Describe the morphology of the red blood cells.
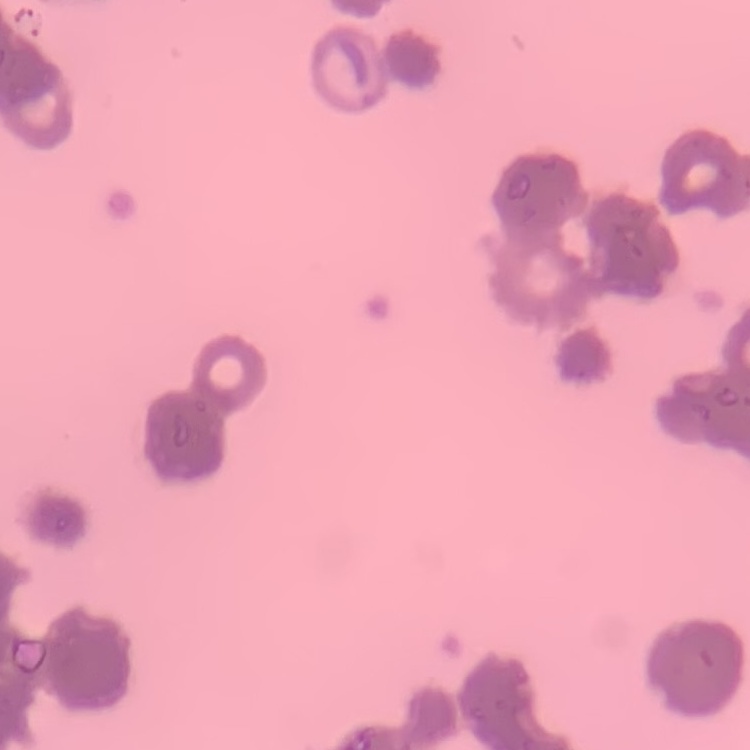

They show rouleaux formation.

Field's or Giemsa stain. One tile cut from a larger photomicrograph. Thin blood smear.